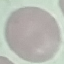

malaria status = uninfected
stain = Giemsa
preparation = thin blood smear
capture = smartphone camera at the microscope eyepiece
image type = automatically extracted cell patch, resized to 64 × 64 pixels